State the preparation type.
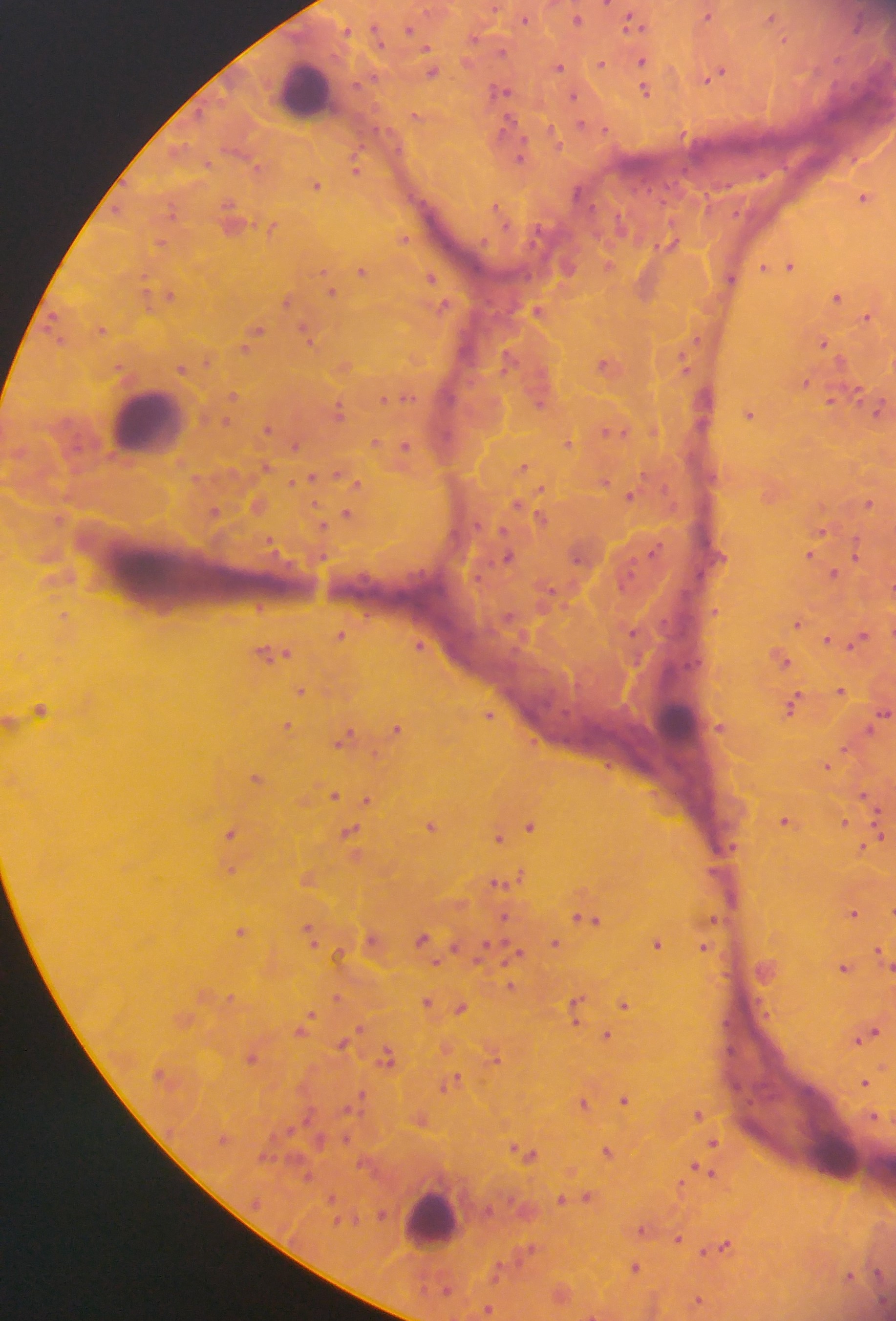
Thick blood film.

Approximate centers as (x, y) in pixels. Leukocyte locations: (305, 91), (148, 420), (676, 720), (835, 1158), (430, 1219). Malaria parasite locations: (708, 14), (773, 16), (576, 17), (525, 18), (634, 20), (410, 28), (642, 61), (601, 64), (559, 66), (432, 70), (644, 70), (718, 73), (646, 89), (501, 90), (574, 96), (416, 116), (581, 125), (521, 156), (356, 169), (317, 184), (865, 197), (232, 221), (273, 225), (404, 239), (161, 243), (671, 243), (608, 265), (789, 265), (765, 266), (362, 270), (431, 277), (730, 277), (645, 288), (331, 290), (168, 294), (837, 296), (287, 299), (537, 309), (869, 316), (102, 329), (255, 333), (308, 335), (824, 343), (509, 358), (345, 364), (607, 364), (684, 365), (182, 368), (805, 382), (233, 396), (405, 397), (384, 398), (834, 398), (540, 400), (339, 410), (879, 410), (750, 413), (268, 428), (615, 431), (376, 441), (569, 443), (295, 444), (406, 446), (524, 466), (310, 479), (605, 480), (630, 495), (869, 503), (524, 507), (215, 512), (347, 513), (541, 516), (822, 531), (856, 553), (810, 555), (508, 557), (834, 573), (260, 607), (798, 623), (633, 631), (342, 635), (859, 638), (828, 640), (420, 645), (273, 653), (781, 658), (302, 690), (841, 690), (793, 705), (41, 709), (883, 713), (490, 714), (287, 724), (719, 727), (397, 728), (345, 739), (827, 765), (256, 777), (333, 794), (367, 799), (869, 799), (786, 821), (844, 822), (531, 825), (431, 826), (351, 831), (232, 832), (499, 837), (874, 838), (230, 869), (517, 876), (308, 878), (500, 883), (853, 912), (504, 917), (587, 919), (714, 919), (241, 931), (311, 932), (424, 938), (373, 939), (556, 943), (657, 943), (705, 946), (516, 952), (882, 953), (845, 967), (512, 986), (337, 998), (427, 1001), (625, 1003), (577, 1006), (461, 1008), (310, 1015), (305, 1023), (607, 1036), (866, 1036), (345, 1041), (446, 1048), (387, 1056), (495, 1056), (253, 1057), (452, 1080), (865, 1082), (625, 1099), (584, 1102), (698, 1114), (420, 1119), (714, 1142), (525, 1152), (609, 1152), (705, 1172), (681, 1184), (576, 1197), (587, 1197), (562, 1199), (382, 1215), (643, 1229), (678, 1238), (722, 1246), (529, 1249), (635, 1266), (851, 1275), (562, 1293), (699, 1300), (488, 1308), (591, 1315). Photographed through a microscope with a mobile-phone camera. One field of view. Collected in Ghana. Image is 896×1321 pixels.